State which cell type is depicted.
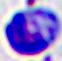
A leukocyte.

Summary:
  - Magnification: 400x
  - Modality: photomicrograph